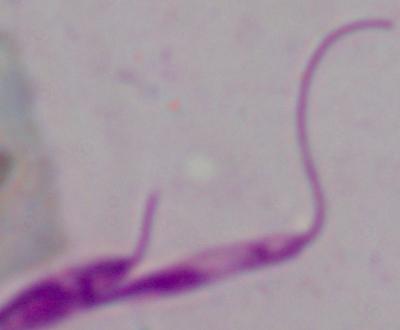

Summary:
  - Identification: Leishmania
  - Magnification: 1000x
  - Modality: micrograph